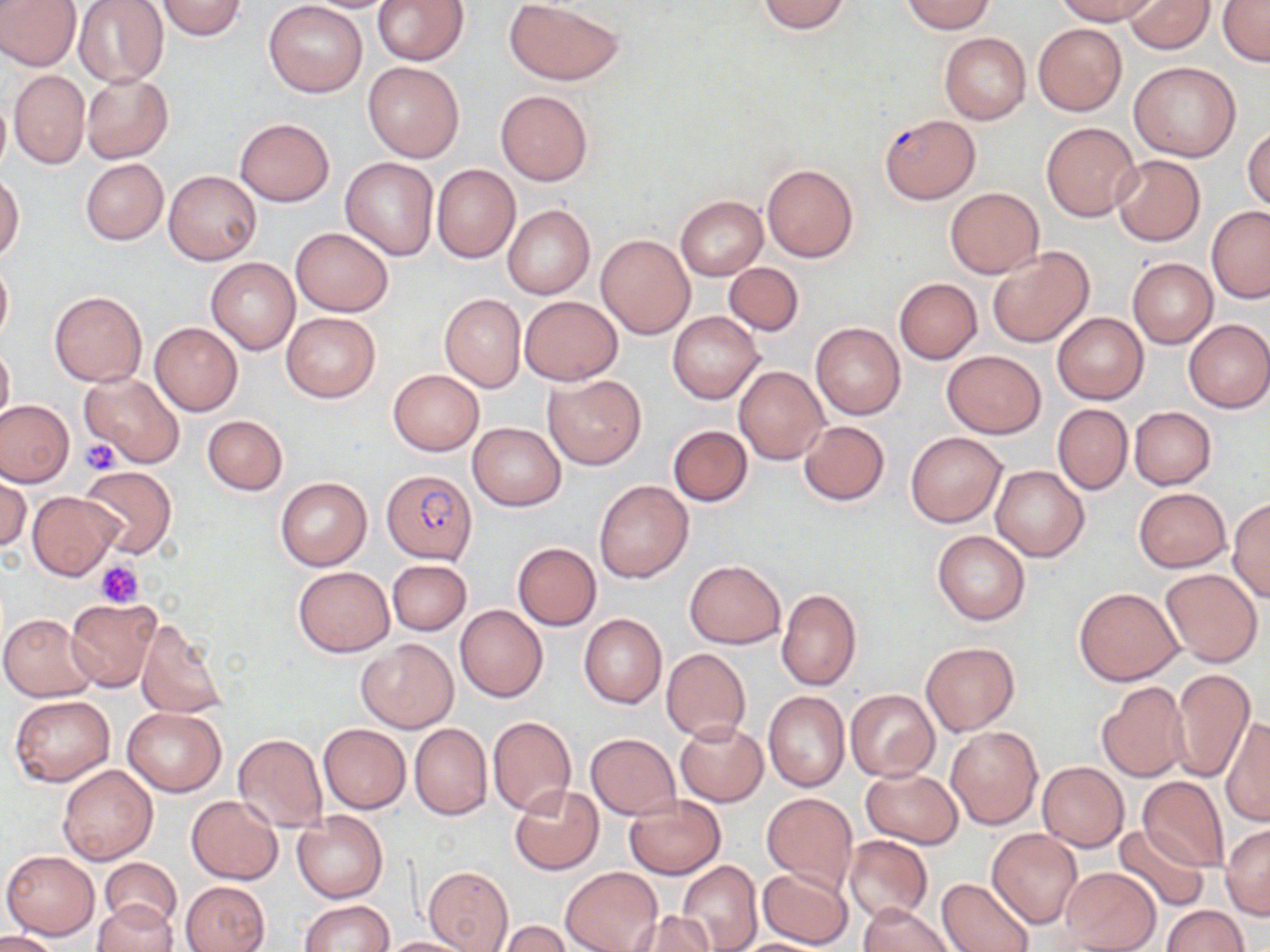
Summary:
  - Coordinate format: approximate bounding boxes as [x1, y1, x2, y2] in pixels
  - Uninfected red blood cell locations: [0, 0, 81, 72], [153, 0, 249, 40], [300, 0, 403, 13], [371, 0, 469, 66], [756, 0, 853, 33], [1054, 0, 1159, 25], [1125, 0, 1215, 54], [1218, 0, 1270, 67], [72, 1, 168, 88], [503, 1, 623, 85], [900, 1, 997, 33], [263, 2, 367, 98], [1034, 23, 1127, 116], [939, 33, 1031, 123], [1128, 61, 1241, 162], [363, 62, 464, 161], [9, 70, 89, 169], [81, 73, 173, 164], [495, 89, 593, 186], [0, 90, 10, 181], [235, 119, 334, 205], [1040, 122, 1140, 221], [1243, 123, 1270, 212], [1110, 154, 1206, 246], [340, 157, 439, 261], [81, 159, 167, 244], [762, 164, 859, 262], [431, 165, 520, 263], [164, 170, 261, 264], [0, 174, 24, 261], [944, 186, 1043, 279], [675, 196, 767, 280], [502, 205, 595, 299], [1207, 206, 1269, 301], [290, 227, 394, 317], [597, 235, 694, 338], [987, 246, 1095, 347], [0, 257, 13, 346], [206, 257, 300, 354], [1127, 258, 1216, 347], [724, 262, 803, 336], [894, 278, 982, 363], [49, 291, 147, 387], [439, 294, 525, 392], [518, 295, 623, 386], [282, 311, 379, 403], [668, 311, 764, 405], [1052, 312, 1148, 404], [1183, 319, 1269, 413], [150, 323, 242, 415], [812, 323, 905, 419], [0, 341, 13, 428], [941, 350, 1046, 437], [734, 365, 829, 464], [387, 369, 484, 456], [80, 373, 186, 468], [545, 373, 646, 470], [0, 399, 74, 488], [1052, 403, 1132, 495], [1129, 406, 1216, 489], [202, 415, 287, 495], [798, 420, 889, 505], [468, 422, 565, 510], [668, 425, 753, 506], [905, 431, 1006, 527], [990, 463, 1088, 561], [80, 465, 177, 557], [1, 474, 30, 553], [275, 476, 371, 571], [594, 480, 692, 583], [1132, 486, 1232, 573], [27, 490, 123, 580], [1227, 498, 1270, 601], [932, 529, 1030, 625], [513, 542, 601, 630], [684, 559, 785, 648], [387, 560, 471, 635], [293, 565, 395, 657], [1160, 569, 1262, 667], [1074, 586, 1182, 684], [776, 588, 862, 691], [66, 596, 163, 692], [455, 605, 549, 703], [1, 613, 99, 701], [579, 614, 666, 709], [135, 618, 227, 719], [356, 639, 458, 733], [921, 641, 1020, 736], [661, 648, 750, 742], [1170, 669, 1254, 781], [1096, 683, 1190, 783], [845, 689, 939, 782], [763, 692, 849, 791], [8, 696, 115, 787], [123, 708, 226, 796], [487, 716, 575, 816], [1222, 719, 1269, 826], [675, 721, 767, 806], [318, 723, 411, 813], [409, 723, 492, 820], [945, 726, 1041, 828], [233, 733, 327, 834], [586, 733, 679, 818], [1037, 761, 1128, 850], [58, 764, 157, 865], [860, 767, 962, 848], [1137, 776, 1227, 872], [508, 786, 604, 875], [762, 792, 858, 893], [186, 795, 282, 884], [623, 796, 726, 878], [291, 810, 387, 903], [1114, 823, 1208, 912], [1221, 824, 1270, 919], [988, 829, 1083, 927], [845, 836, 932, 924], [2, 849, 99, 939], [101, 858, 181, 929], [677, 861, 762, 952], [423, 865, 513, 952], [559, 866, 662, 952], [756, 867, 853, 949], [1059, 867, 1162, 951], [936, 877, 1034, 951], [182, 881, 269, 952], [297, 900, 393, 952], [91, 902, 178, 952], [857, 903, 958, 952], [1161, 905, 1248, 952], [625, 912, 717, 952], [497, 921, 573, 952], [0, 931, 58, 951], [377, 936, 474, 951], [729, 937, 837, 951]
  - Plasmodium falciparum-infected red blood cell locations: [878, 114, 980, 203], [382, 468, 477, 564]
  - Platelet locations: [81, 438, 120, 474], [97, 559, 145, 608]
  - Slide-level diagnosis: Plasmodium falciparum
  - Preparation: thin blood film
  - Field of view: single
  - Modality: light microscopy
  - Image size: 1270×952 pixels
  - Stain: May-Grünwald-Giemsa
  - Magnification: 1000x